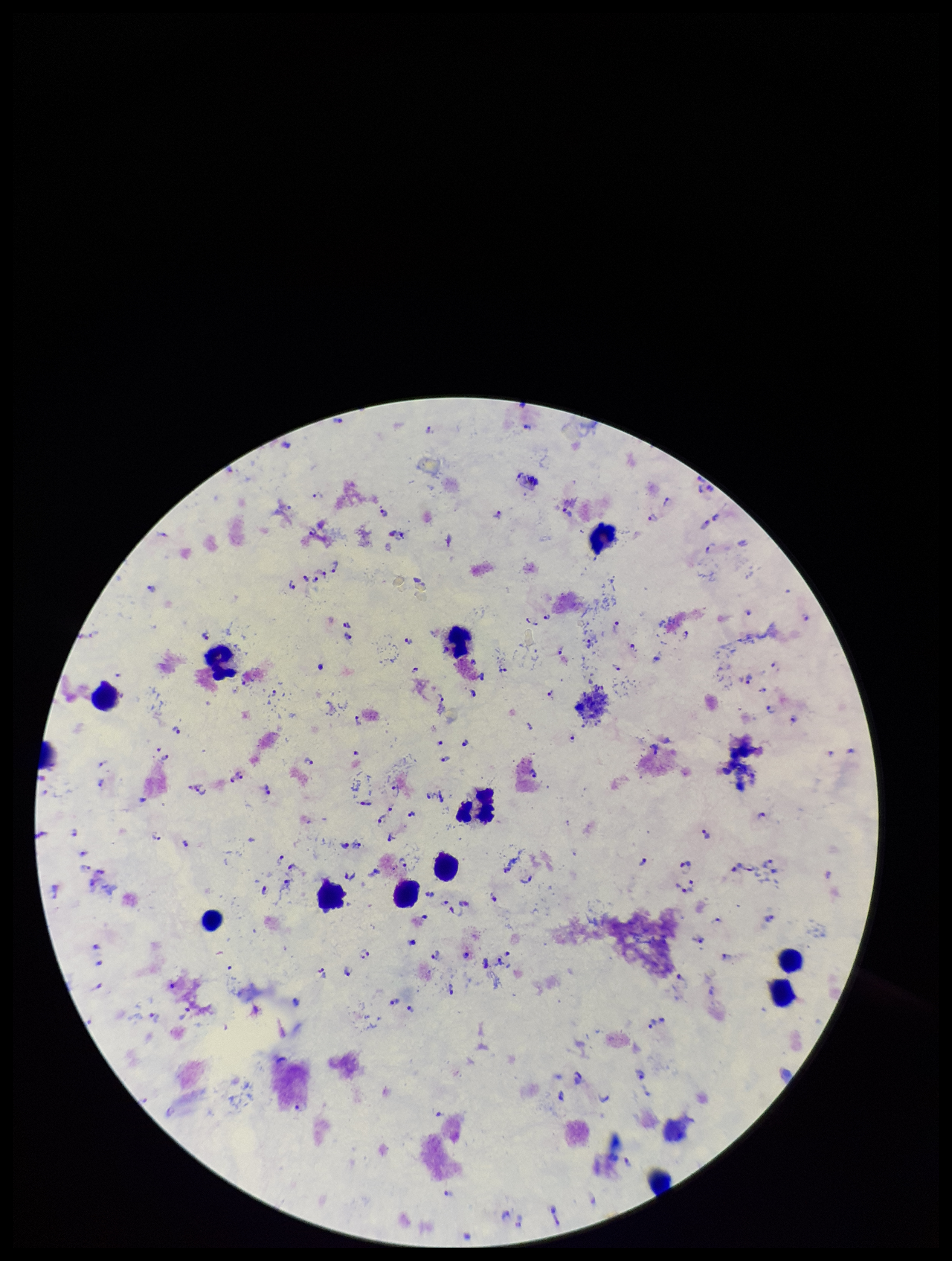

Summary:
  - Patient malaria status: positive
  - Stain: Giemsa
  - Species reported for this patient: Plasmodium falciparum
  - Parasite count: 91
  - Plasmodium parasites: detected
  - Capture: smartphone photograph through the microscope eyepiece
  - Preparation: thick blood smear
  - Image size: 952×1261 pixels
  - Leukocyte count: 13
  - Field of view: one from this slide